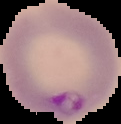
image type = segmented cell region on a black background
preparation = thin blood film
result = malaria parasites detected
image size = 121×124 pixels